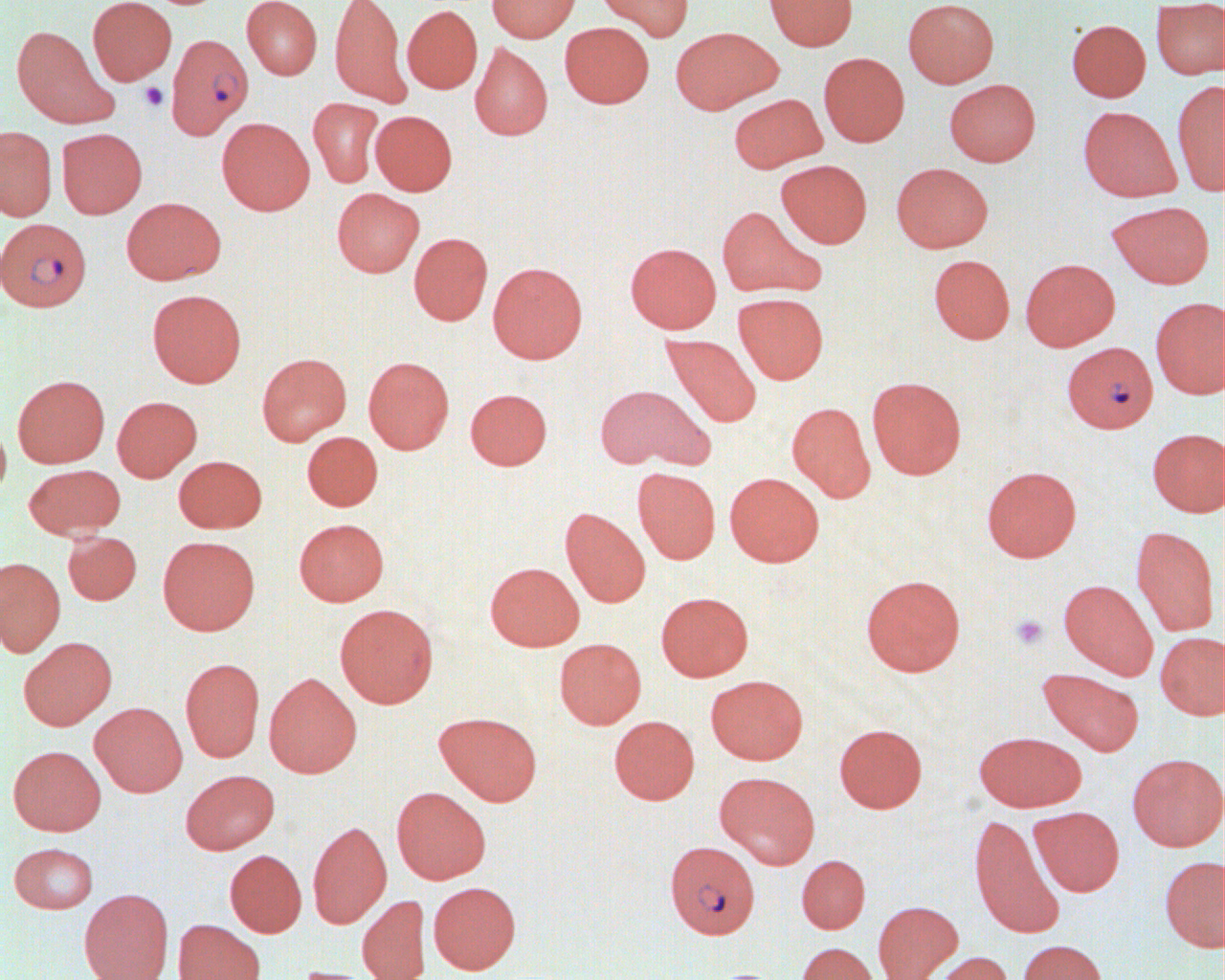
Summary:
  - Coordinate format: approximate bounding boxes as (x1,y1)-(x2,y2) corner pairs in pixels
  - Platelet locations: (140,82)-(169,111), (1009,614)-(1049,651)
  - Plasmodium falciparum-infected red blood cell locations: (166,35)-(254,139), (1,218)-(91,311), (1068,340)-(1164,435), (665,840)-(760,938)
  - Uninfected red blood cell locations: (88,0)-(176,85), (242,0)-(322,80), (329,0)-(412,109), (487,0)-(580,42), (596,0)-(693,41), (764,0)-(858,51), (903,0)-(999,88), (1151,4)-(1225,80), (402,5)-(483,94), (1067,19)-(1151,102), (560,22)-(654,108), (11,25)-(118,129), (669,26)-(781,114), (469,42)-(553,141), (818,52)-(909,146), (945,79)-(1040,166), (1171,79)-(1224,196), (729,93)-(827,172), (308,97)-(384,188), (1078,106)-(1182,202), (370,110)-(457,195), (216,117)-(314,215), (0,126)-(57,221), (57,128)-(147,218), (776,159)-(872,248), (891,162)-(994,252), (332,188)-(423,277), (121,197)-(226,284), (1106,200)-(1214,289), (716,205)-(826,299), (409,232)-(492,325), (625,242)-(722,333), (928,254)-(1015,344), (1020,258)-(1119,351), (487,261)-(587,363), (147,289)-(246,387), (733,293)-(828,384), (1150,298)-(1225,399), (660,333)-(762,429), (256,353)-(352,446), (363,356)-(454,453), (12,374)-(110,467), (866,376)-(966,479), (593,384)-(709,471), (465,388)-(552,470), (112,395)-(202,482), (786,401)-(876,502), (0,419)-(11,499), (1147,428)-(1225,517), (302,431)-(383,511), (173,455)-(266,532), (23,464)-(125,539), (981,466)-(1082,562), (632,468)-(720,564), (724,472)-(824,567), (560,507)-(651,607), (294,518)-(389,606), (1130,526)-(1220,636), (62,531)-(141,605), (157,536)-(260,634), (0,557)-(66,657), (484,562)-(584,651), (861,574)-(965,676), (1058,579)-(1158,680), (656,591)-(753,681), (334,603)-(439,708), (1155,631)-(1225,720), (18,636)-(117,730), (554,637)-(646,729), (180,657)-(265,762), (1037,668)-(1144,756), (264,672)-(361,777), (705,674)-(808,764), (89,702)-(187,796), (434,711)-(542,805), (609,716)-(699,804), (834,723)-(927,812), (973,730)-(1086,811), (8,745)-(105,835), (1127,753)-(1224,851), (180,769)-(279,854), (715,771)-(820,869), (391,786)-(490,884), (1029,806)-(1124,896), (968,814)-(1065,938), (307,821)-(392,928), (9,842)-(98,913), (224,849)-(306,937), (796,854)-(870,933), (1159,854)-(1225,952), (428,881)-(521,973), (79,888)-(174,980), (357,895)-(430,980), (873,900)-(962,980), (173,919)-(265,980), (1017,939)-(1107,980), (796,942)-(880,980), (932,951)-(1014,980), (289,966)-(378,980)
  - Slide-level diagnosis: Plasmodium falciparum
  - Modality: light microscopy
  - Field of view: single
  - Preparation: thin blood film
  - Magnification: 1000x
  - Image size: 1225×980 pixels